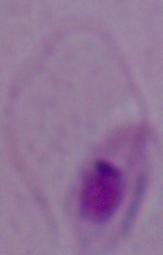

Summary:
  - Modality: micrograph
  - Magnification: 1000x
  - Identification: Leishmania